Name the parasite shown.
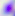

Toxoplasma gondii.

magnification = 400x
modality = micrograph